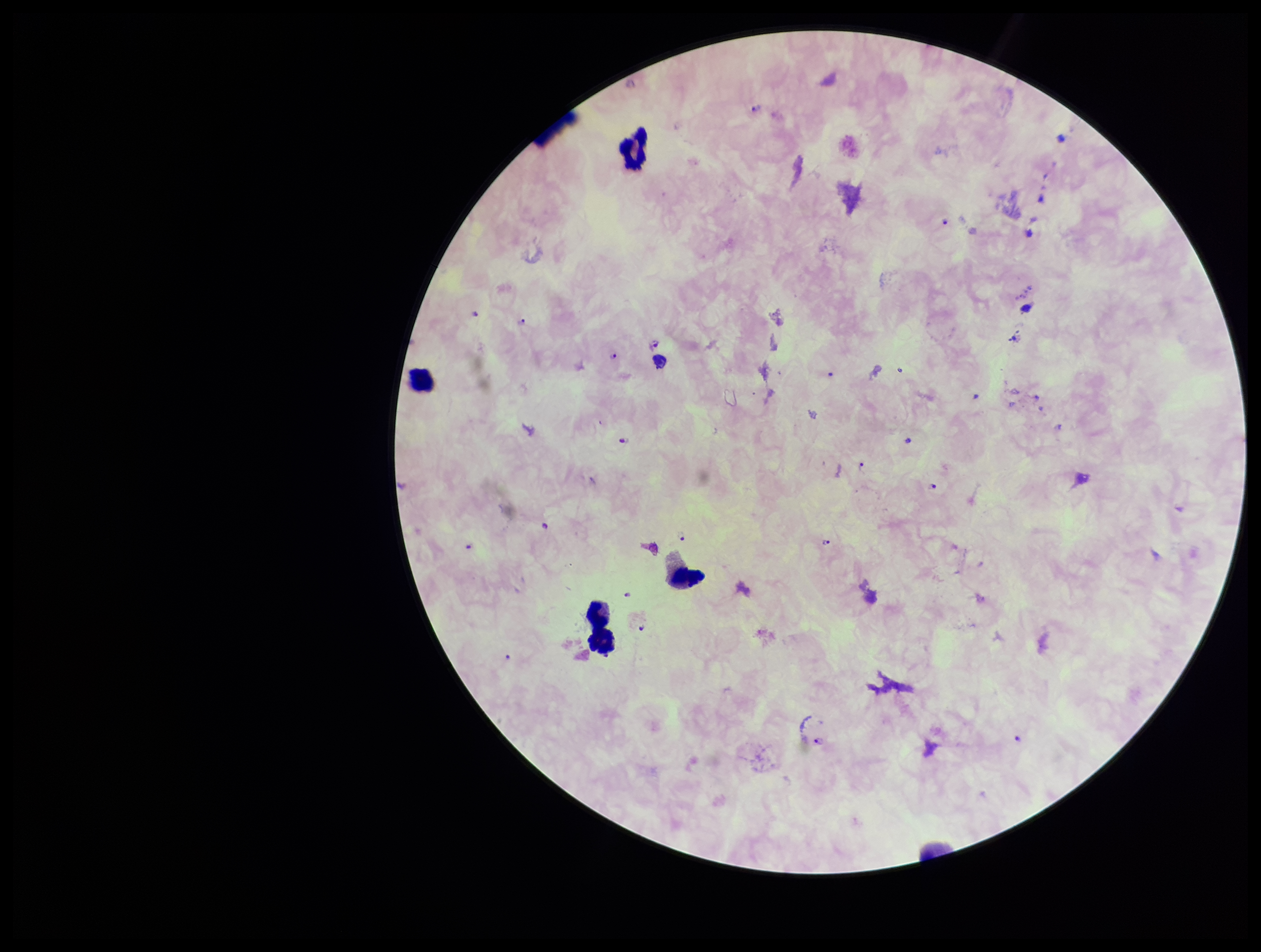
field of view = single
species reported for this patient = Plasmodium falciparum
parasite count = 18
stain = Giemsa
Plasmodium parasites = identified
image size = 1261×952 pixels
preparation = thick smear
leukocyte count = 4
patient malaria status = positive
capture = smartphone photograph through the microscope eyepiece